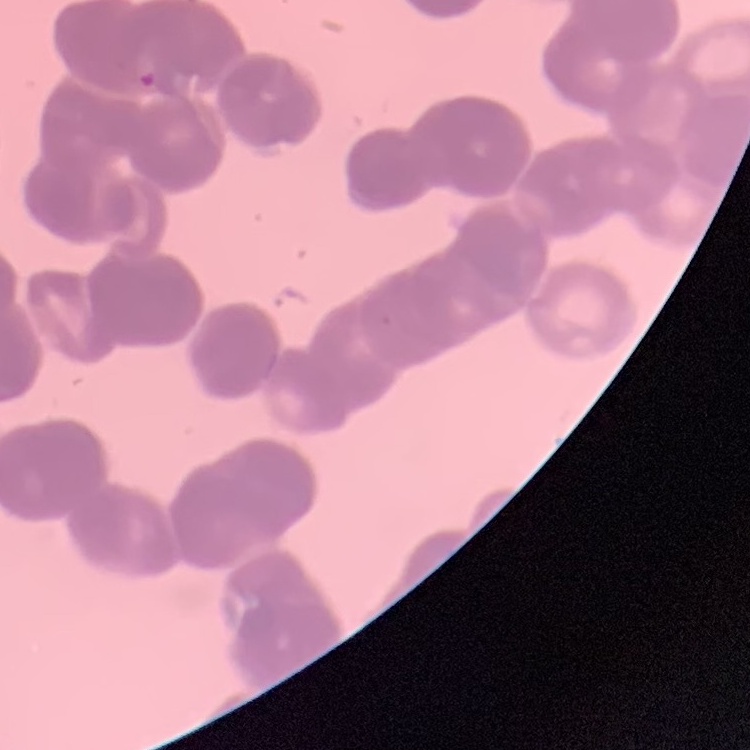

Summary:
  - Erythrocyte morphology: rouleaux formation
  - Preparation: thin peripheral smear
  - Image type: square crop of a larger photomicrograph
  - Stain: Field's or Giemsa